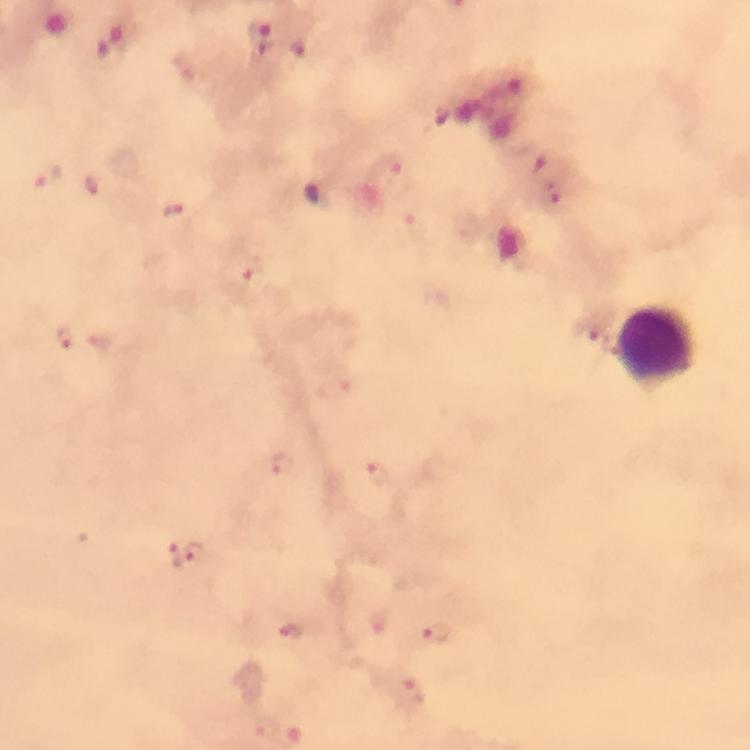
context = from a diagnostic examination for malaria
cropped from = a single field of view
immersion oil = used
magnification = 100x
stain = Giemsa
image size = 750×750 pixels
Plasmodium parasite locations = approximate centers as (x, y) in pixels: (399, 177), (48, 179), (93, 184), (172, 208), (245, 274), (62, 339), (100, 343), (285, 466), (376, 473), (195, 552), (177, 555), (377, 623), (291, 632), (437, 632), (413, 692), (263, 726)
leukocyte locations = approximate centers as (x, y) in pixels: (654, 348)
preparation = thick smear
capture = smartphone mounted on the microscope